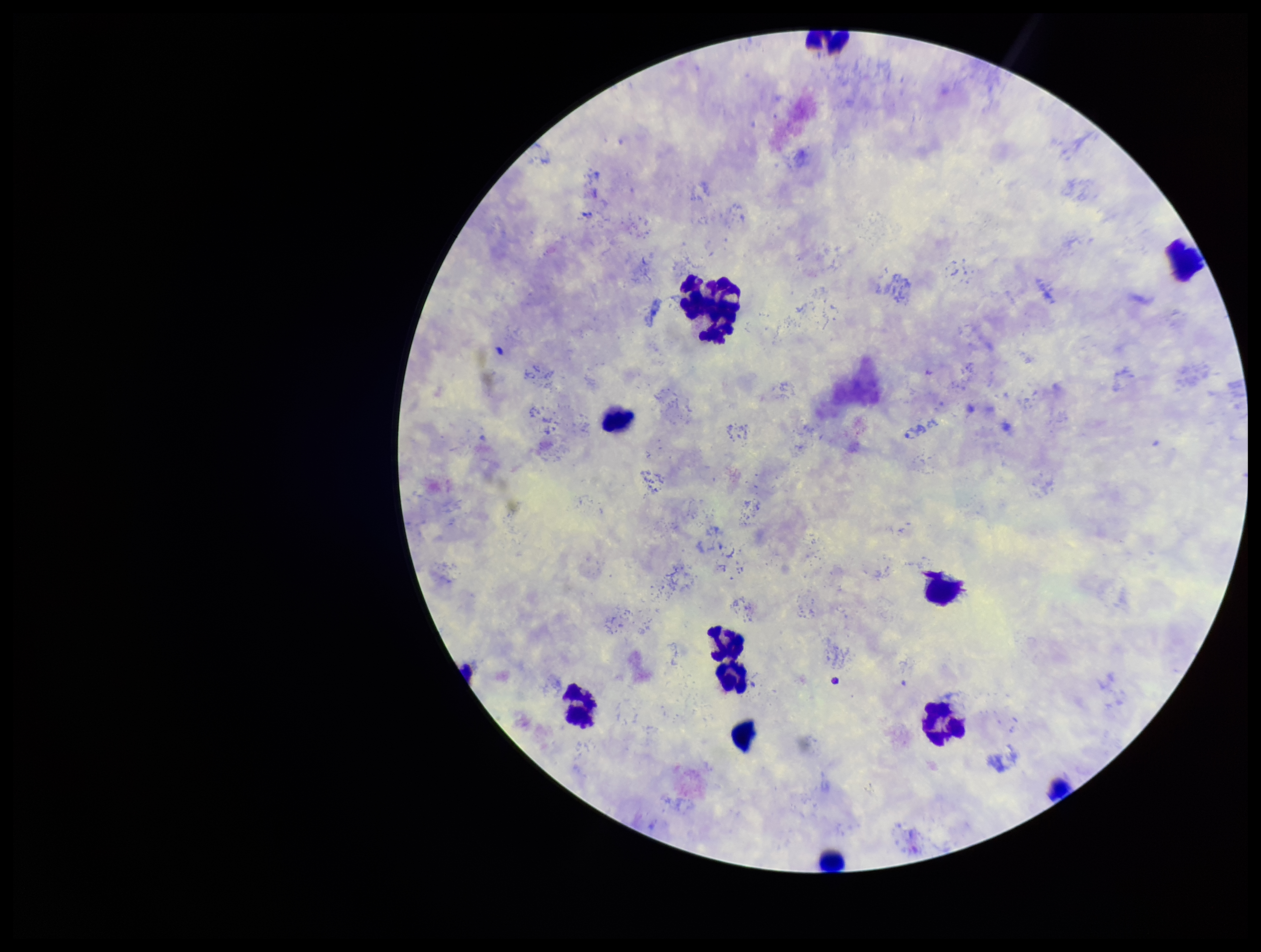
preparation = thick smear
field of view = single
capture = smartphone photograph through the microscope eyepiece
leukocyte count = 12
parasite count = 0
stain = Giemsa
Plasmodium parasites = none seen
patient malaria status = infected
image size = 1261×952 pixels
species reported for this patient = Plasmodium vivax